Classify this cell by malaria status.
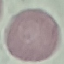

Uninfected.

Summary:
  - Capture: smartphone through the microscope eyepiece
  - Preparation: thin blood film
  - Stain: Giemsa
  - Image type: cell patch, automatically extracted from a larger field of view and resized to 64 × 64 pixels